Classify this cell by malaria status.
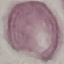
It is uninfected.

Cell patch, automatically extracted from a larger field of view and resized to 64 × 64 pixels. Photographed with a smartphone camera at the microscope eyepiece. Thin smear of blood. Giemsa-stained preparation.